Assess the morphology of the erythrocytes.
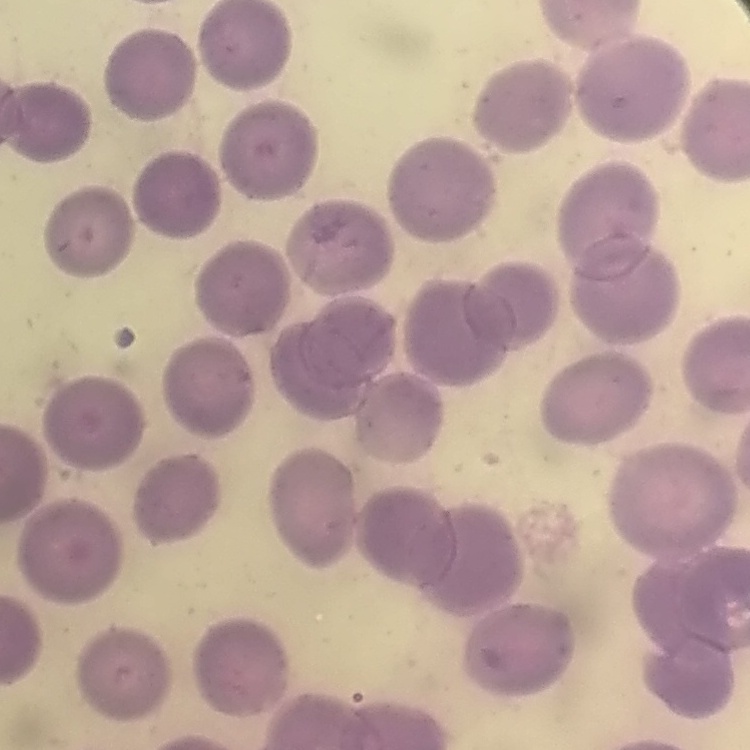

They show no rouleaux formation.

{
  "image_type": "square crop of a larger photomicrograph",
  "stain": "Field's or Giemsa",
  "preparation": "thin peripheral smear"
}